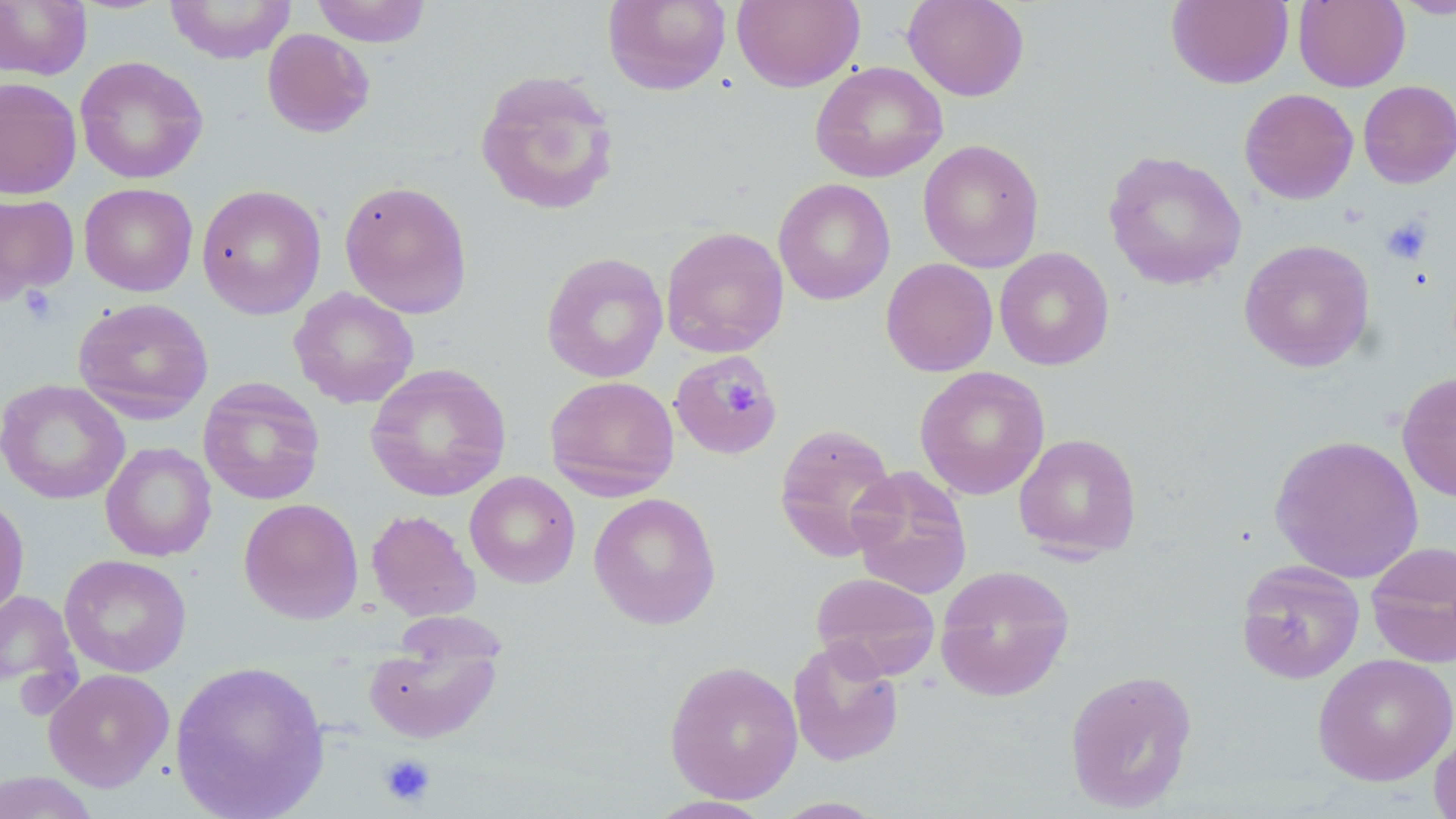

Approximate bounding boxes as (x1, y1, x2, y2) in pixels. Uninfected red blood cell locations: (164, 0, 298, 64), (311, 0, 433, 47), (732, 0, 864, 92), (902, 0, 1029, 101), (1166, 0, 1293, 89), (1293, 0, 1410, 92), (1391, 0, 1456, 20), (0, 1, 92, 80), (602, 1, 732, 95), (262, 28, 375, 137), (74, 55, 208, 184), (810, 60, 948, 183), (474, 68, 621, 217), (0, 77, 82, 200), (1358, 80, 1456, 188), (1239, 88, 1358, 205), (918, 139, 1045, 273), (1103, 150, 1247, 291), (773, 178, 895, 305), (339, 180, 473, 319), (80, 182, 197, 297), (196, 184, 327, 319), (0, 193, 79, 304), (660, 226, 789, 358), (1238, 239, 1375, 371), (994, 247, 1114, 370), (541, 252, 668, 383), (881, 259, 998, 376), (289, 287, 419, 408), (73, 297, 213, 423), (669, 349, 783, 461), (365, 363, 512, 502), (914, 366, 1050, 500), (1397, 371, 1456, 502), (544, 375, 680, 500), (198, 378, 326, 505), (0, 379, 130, 505), (774, 423, 899, 561), (1013, 433, 1142, 560), (1268, 434, 1425, 583), (100, 442, 217, 561), (847, 465, 973, 599), (464, 471, 581, 588), (588, 492, 721, 630), (0, 495, 30, 622), (238, 498, 364, 624), (366, 509, 480, 621), (1365, 541, 1456, 668), (59, 554, 192, 678), (1236, 559, 1365, 684), (935, 564, 1075, 701), (810, 572, 941, 680), (0, 589, 80, 703), (363, 636, 504, 744), (787, 637, 905, 767), (1313, 653, 1456, 786), (169, 660, 330, 818), (663, 660, 803, 803), (43, 668, 175, 792), (1064, 668, 1198, 813), (1429, 728, 1456, 819), (0, 771, 102, 819), (646, 796, 775, 818), (769, 796, 890, 818). Platelet locations: (1380, 215, 1432, 265), (18, 286, 59, 327), (715, 377, 761, 416), (378, 753, 437, 808). Slide-level diagnosis: negative for blood parasites. May-Grünwald-Giemsa stain. Thin blood smear. 1000x magnification. One field of a larger specimen. Image is 1456×819 pixels. Light microscopy.